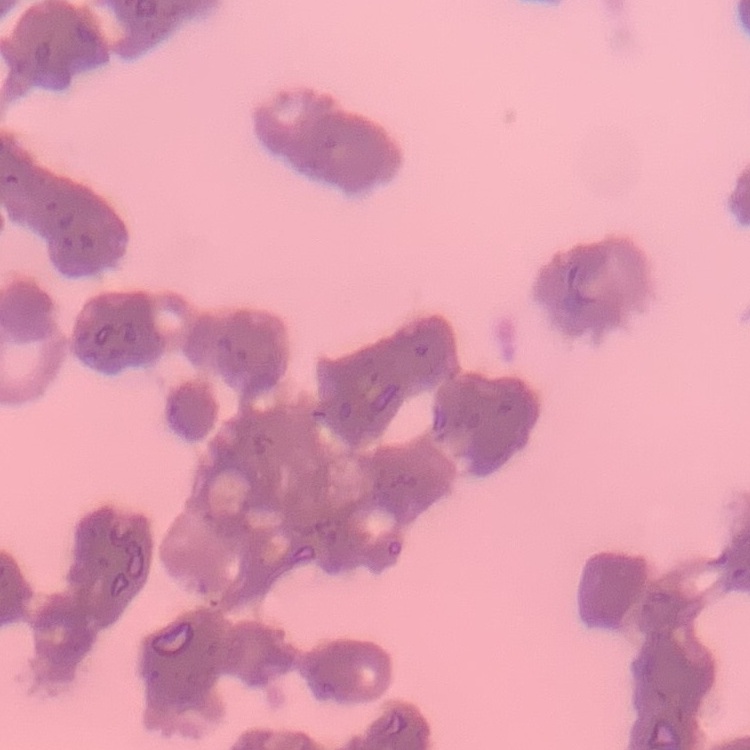
The erythrocytes show rouleaux formation. Square crop of a larger photomicrograph. Thin blood smear. Stained with either Field's or Giemsa.